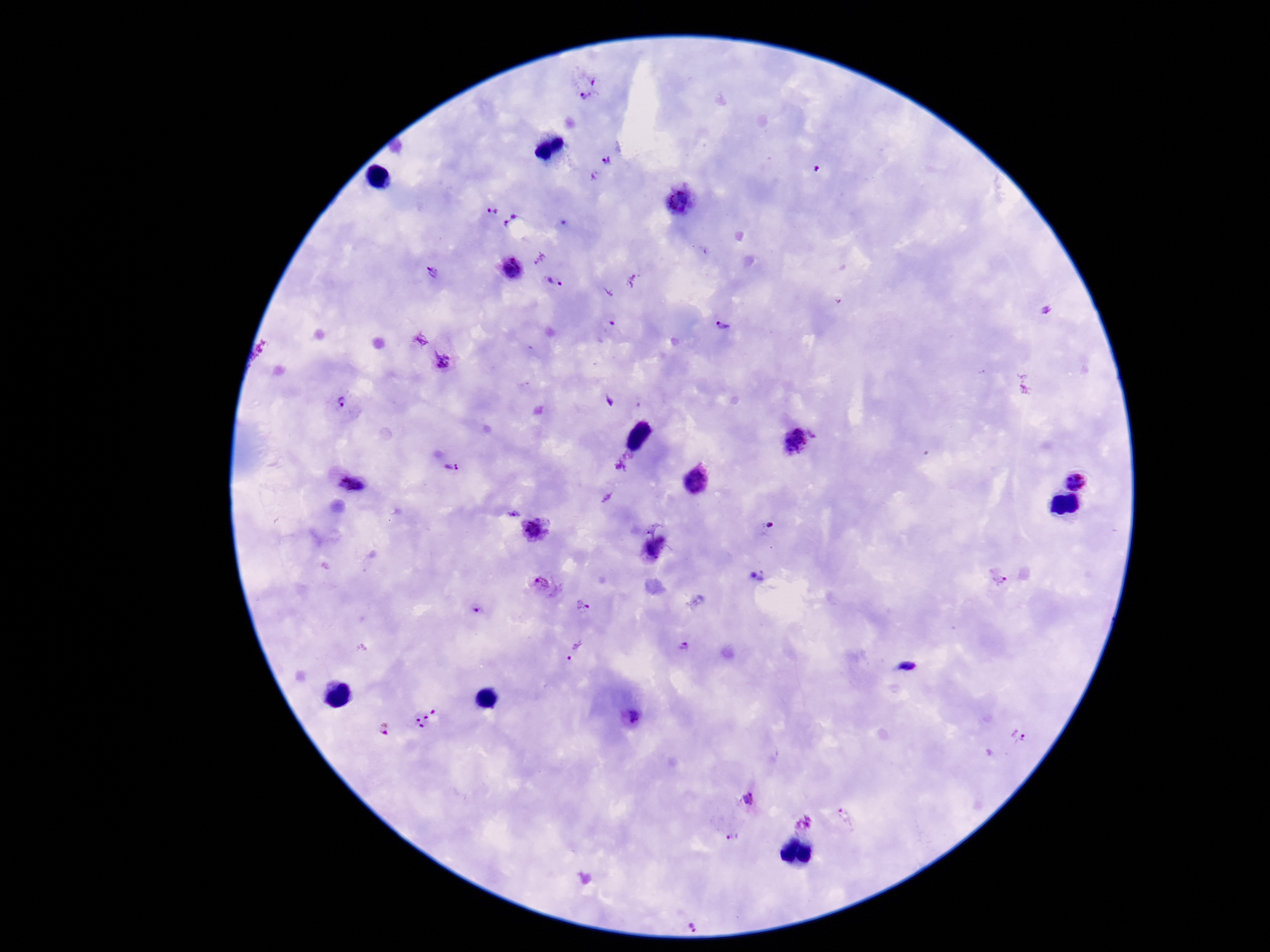

capture = smartphone camera through the microscope eyepiece
field of view = one from this slide
Plasmodium parasite locations = approximate centers as (x, y) in pixels: (584, 85), (607, 162), (680, 199), (491, 211), (514, 223), (511, 270), (434, 272), (554, 281), (725, 327), (446, 361), (341, 402), (793, 439), (451, 468), (349, 479), (1076, 479), (512, 514), (537, 529), (999, 580), (545, 586), (584, 607), (479, 612), (684, 648), (575, 649), (427, 717), (629, 717), (383, 729), (1018, 736), (747, 798), (848, 817), (804, 823), (731, 837), (696, 925)
stain = Giemsa
patient malaria status = positive
magnification = 100x
image size = 1270×952 pixels
preparation = thick blood film